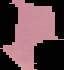
image type = segmented cell region with the area outside set to black
malaria status = uninfected
image size = 64×70 pixels
preparation = thin blood film